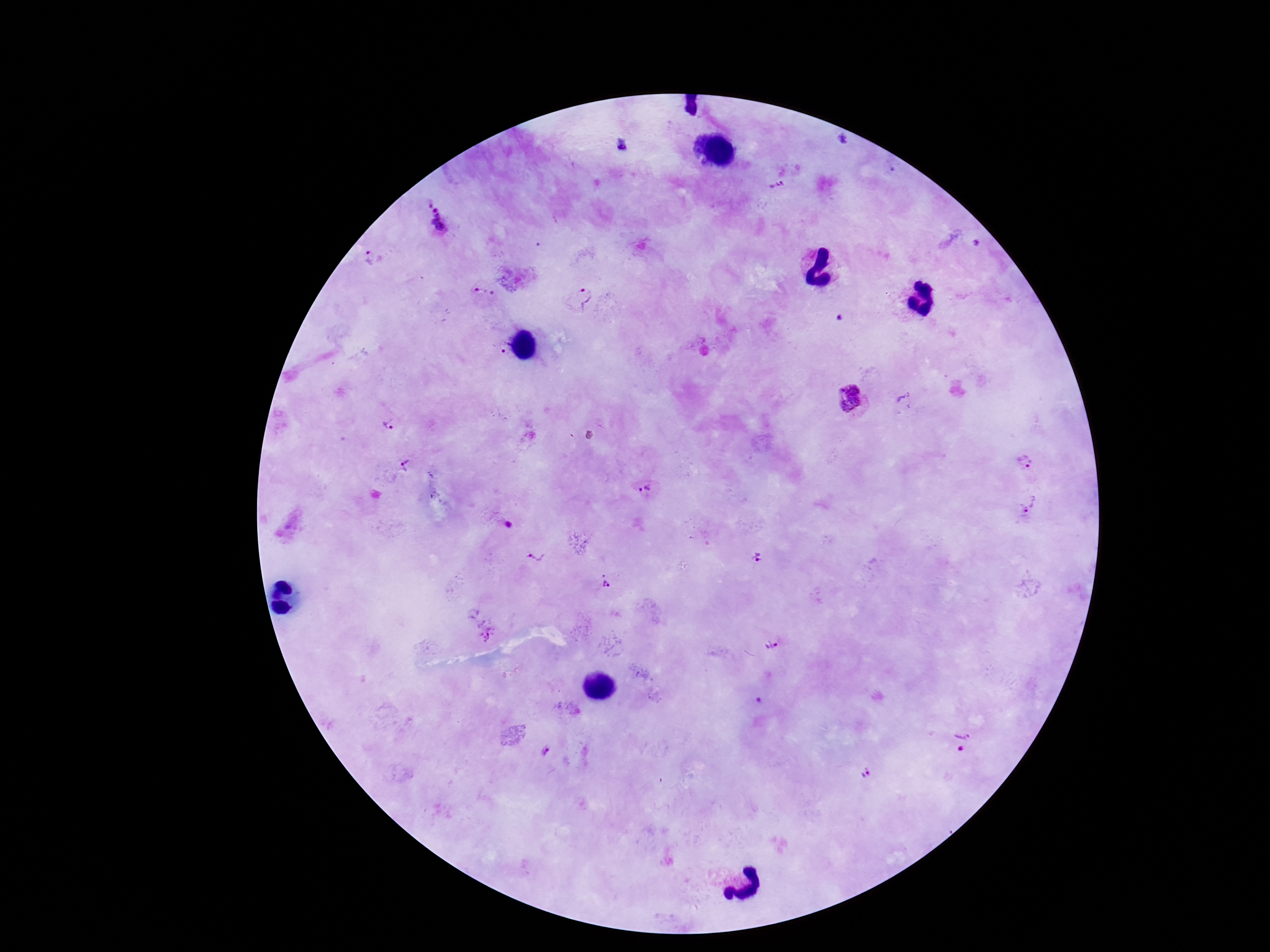

Approximate centers as [x, y] in pixels.
Summary:
  - Plasmodium parasite locations: [623, 146], [777, 184], [435, 221], [371, 259], [484, 294], [582, 297], [852, 397], [388, 425], [1026, 461], [406, 465], [644, 490], [1031, 506], [508, 524], [535, 556], [759, 558], [606, 581], [486, 631], [771, 644], [962, 740], [545, 751], [866, 773]
  - Capture: smartphone camera through the microscope eyepiece
  - Patient malaria status: positive
  - Stain: Giemsa
  - Field of view: one from this slide
  - Preparation: thick blood film
  - Image size: 1270×952 pixels
  - Magnification: 100x